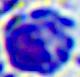 400x magnification. A leukocyte is shown. Photomicrograph.